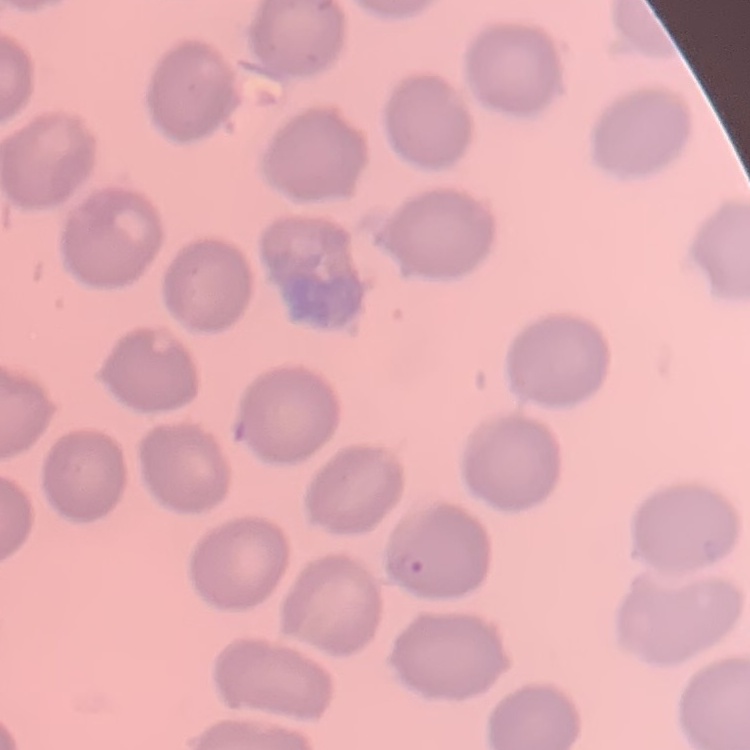

Summary:
  - Red blood cell morphology: no rouleaux formation
  - Stain: Field's or Giemsa
  - Image type: square crop of a larger photomicrograph
  - Preparation: thin blood film